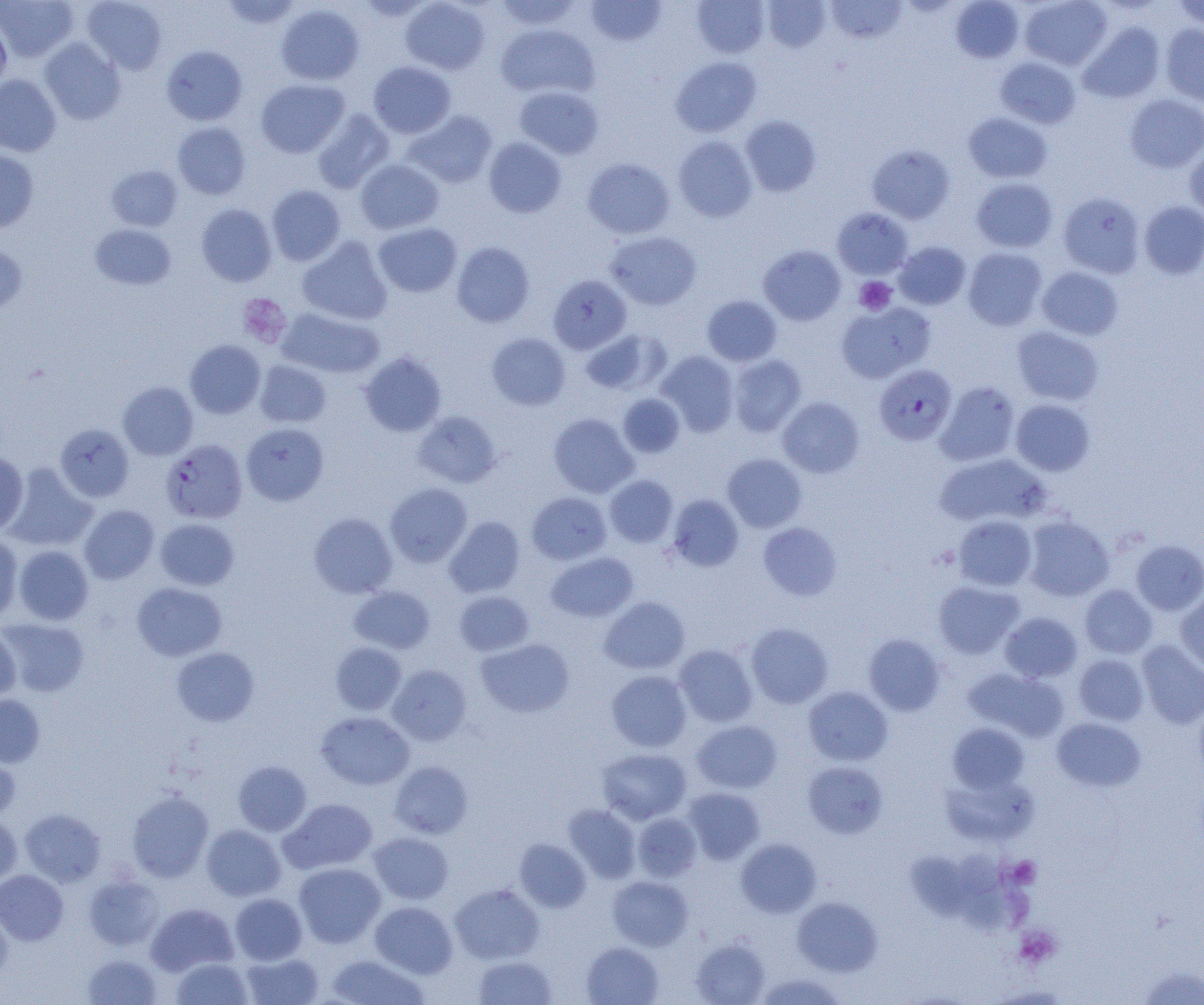
Summary:
  - Coordinate format: approximate bounding boxes as named x1/y1/x2/y2 corners in pixels
  - Uninfected red blood cell locations: (x1=0, y1=0, x2=78, y2=62), (x1=81, y1=0, x2=168, y2=73), (x1=219, y1=0, x2=302, y2=30), (x1=400, y1=0, x2=490, y2=75), (x1=494, y1=0, x2=581, y2=30), (x1=585, y1=0, x2=667, y2=46), (x1=692, y1=0, x2=769, y2=58), (x1=762, y1=0, x2=831, y2=52), (x1=950, y1=0, x2=1024, y2=63), (x1=1019, y1=0, x2=1112, y2=70), (x1=1171, y1=0, x2=1204, y2=29), (x1=826, y1=1, x2=907, y2=44), (x1=276, y1=4, x2=364, y2=86), (x1=0, y1=16, x2=11, y2=93), (x1=1079, y1=22, x2=1165, y2=103), (x1=495, y1=24, x2=599, y2=99), (x1=1160, y1=24, x2=1204, y2=106), (x1=39, y1=38, x2=126, y2=125), (x1=161, y1=45, x2=247, y2=125), (x1=671, y1=56, x2=761, y2=137), (x1=995, y1=57, x2=1081, y2=129), (x1=368, y1=61, x2=456, y2=138), (x1=0, y1=74, x2=61, y2=156), (x1=256, y1=79, x2=349, y2=157), (x1=514, y1=86, x2=603, y2=159), (x1=1125, y1=94, x2=1204, y2=173), (x1=312, y1=109, x2=395, y2=193), (x1=403, y1=110, x2=498, y2=188), (x1=963, y1=111, x2=1053, y2=183), (x1=740, y1=115, x2=821, y2=196), (x1=172, y1=122, x2=251, y2=200), (x1=673, y1=136, x2=758, y2=222), (x1=483, y1=137, x2=567, y2=218), (x1=1185, y1=142, x2=1204, y2=220), (x1=866, y1=143, x2=955, y2=224), (x1=0, y1=148, x2=38, y2=233), (x1=582, y1=157, x2=675, y2=239), (x1=356, y1=159, x2=444, y2=234), (x1=106, y1=164, x2=183, y2=231), (x1=971, y1=177, x2=1057, y2=252), (x1=266, y1=185, x2=346, y2=265), (x1=1058, y1=192, x2=1145, y2=277), (x1=1139, y1=201, x2=1204, y2=279), (x1=196, y1=203, x2=277, y2=287), (x1=832, y1=208, x2=913, y2=279), (x1=373, y1=222, x2=462, y2=297), (x1=89, y1=224, x2=176, y2=290), (x1=605, y1=230, x2=702, y2=310), (x1=297, y1=236, x2=393, y2=325), (x1=0, y1=241, x2=28, y2=314), (x1=894, y1=241, x2=971, y2=310), (x1=451, y1=242, x2=535, y2=328), (x1=758, y1=244, x2=846, y2=326), (x1=963, y1=247, x2=1047, y2=331), (x1=1036, y1=266, x2=1124, y2=340), (x1=549, y1=275, x2=631, y2=354), (x1=702, y1=295, x2=782, y2=366), (x1=836, y1=302, x2=935, y2=383), (x1=278, y1=307, x2=384, y2=379), (x1=1012, y1=326, x2=1104, y2=406), (x1=580, y1=328, x2=671, y2=395), (x1=487, y1=332, x2=570, y2=411), (x1=184, y1=340, x2=266, y2=419), (x1=656, y1=350, x2=739, y2=436), (x1=359, y1=352, x2=447, y2=437), (x1=728, y1=355, x2=806, y2=437), (x1=254, y1=360, x2=331, y2=428), (x1=117, y1=381, x2=198, y2=460), (x1=935, y1=381, x2=1021, y2=466), (x1=618, y1=394, x2=686, y2=458), (x1=777, y1=397, x2=865, y2=478), (x1=1011, y1=399, x2=1095, y2=476), (x1=413, y1=411, x2=502, y2=488), (x1=548, y1=413, x2=638, y2=498), (x1=55, y1=423, x2=134, y2=502), (x1=241, y1=423, x2=329, y2=506), (x1=0, y1=452, x2=28, y2=534), (x1=722, y1=453, x2=807, y2=532), (x1=934, y1=453, x2=1050, y2=528), (x1=4, y1=463, x2=97, y2=551), (x1=604, y1=474, x2=678, y2=548), (x1=385, y1=483, x2=473, y2=567), (x1=527, y1=492, x2=612, y2=564), (x1=667, y1=494, x2=744, y2=572), (x1=79, y1=504, x2=159, y2=584), (x1=309, y1=512, x2=397, y2=598), (x1=953, y1=515, x2=1038, y2=591), (x1=1022, y1=515, x2=1114, y2=601), (x1=445, y1=516, x2=525, y2=597), (x1=154, y1=518, x2=239, y2=590), (x1=758, y1=522, x2=841, y2=600), (x1=0, y1=534, x2=23, y2=622), (x1=1131, y1=540, x2=1204, y2=615), (x1=13, y1=545, x2=94, y2=625), (x1=546, y1=552, x2=638, y2=622), (x1=933, y1=581, x2=1024, y2=658), (x1=131, y1=582, x2=227, y2=661), (x1=1079, y1=585, x2=1157, y2=659), (x1=349, y1=586, x2=435, y2=653), (x1=454, y1=590, x2=534, y2=656), (x1=1176, y1=593, x2=1204, y2=676), (x1=599, y1=596, x2=690, y2=675), (x1=1000, y1=612, x2=1082, y2=683), (x1=1, y1=617, x2=89, y2=697), (x1=746, y1=622, x2=833, y2=708), (x1=0, y1=626, x2=21, y2=703), (x1=863, y1=633, x2=946, y2=716), (x1=476, y1=638, x2=574, y2=718), (x1=1136, y1=640, x2=1204, y2=729), (x1=330, y1=642, x2=406, y2=715), (x1=673, y1=644, x2=758, y2=727), (x1=172, y1=647, x2=259, y2=726), (x1=1074, y1=654, x2=1148, y2=726), (x1=387, y1=664, x2=472, y2=746), (x1=964, y1=668, x2=1069, y2=741), (x1=606, y1=670, x2=692, y2=752), (x1=803, y1=686, x2=893, y2=766), (x1=0, y1=694, x2=45, y2=767), (x1=1194, y1=697, x2=1204, y2=783), (x1=316, y1=711, x2=414, y2=790), (x1=1052, y1=717, x2=1146, y2=792), (x1=692, y1=720, x2=782, y2=793), (x1=947, y1=723, x2=1029, y2=793), (x1=597, y1=748, x2=691, y2=824), (x1=0, y1=753, x2=20, y2=821), (x1=233, y1=760, x2=312, y2=836), (x1=390, y1=761, x2=473, y2=839), (x1=803, y1=761, x2=888, y2=839), (x1=940, y1=773, x2=1039, y2=846), (x1=683, y1=787, x2=765, y2=864), (x1=127, y1=790, x2=214, y2=882), (x1=279, y1=798, x2=377, y2=874), (x1=563, y1=804, x2=640, y2=883), (x1=19, y1=808, x2=106, y2=887), (x1=0, y1=812, x2=21, y2=887), (x1=632, y1=812, x2=702, y2=882), (x1=201, y1=824, x2=285, y2=901), (x1=369, y1=832, x2=454, y2=904), (x1=514, y1=838, x2=591, y2=912), (x1=736, y1=838, x2=821, y2=917), (x1=962, y1=849, x2=999, y2=891), (x1=905, y1=850, x2=970, y2=921), (x1=294, y1=862, x2=385, y2=947), (x1=0, y1=869, x2=68, y2=945), (x1=84, y1=875, x2=165, y2=950), (x1=607, y1=875, x2=693, y2=951), (x1=450, y1=883, x2=544, y2=964), (x1=960, y1=883, x2=1040, y2=931), (x1=230, y1=893, x2=307, y2=964), (x1=792, y1=896, x2=883, y2=976), (x1=370, y1=901, x2=458, y2=978), (x1=146, y1=903, x2=238, y2=976), (x1=0, y1=907, x2=13, y2=983), (x1=690, y1=937, x2=769, y2=1005), (x1=581, y1=941, x2=664, y2=1005), (x1=240, y1=952, x2=324, y2=1005), (x1=82, y1=953, x2=162, y2=1005), (x1=326, y1=954, x2=429, y2=1005), (x1=472, y1=955, x2=558, y2=1004), (x1=171, y1=957, x2=253, y2=1005), (x1=1136, y1=965, x2=1204, y2=1005), (x1=754, y1=973, x2=846, y2=1004)
  - Plasmodium falciparum-infected red blood cell locations: (x1=874, y1=364, x2=956, y2=446), (x1=161, y1=439, x2=248, y2=524)
  - Platelet locations: (x1=855, y1=276, x2=896, y2=315), (x1=237, y1=293, x2=292, y2=348), (x1=1009, y1=856, x2=1041, y2=887), (x1=1015, y1=925, x2=1062, y2=967)
  - Slide-level diagnosis: Plasmodium falciparum
  - Image size: 1204×1005 pixels
  - Field of view: one of a larger specimen
  - Preparation: thin blood smear
  - Magnification: 1000x
  - Modality: optical microscopy